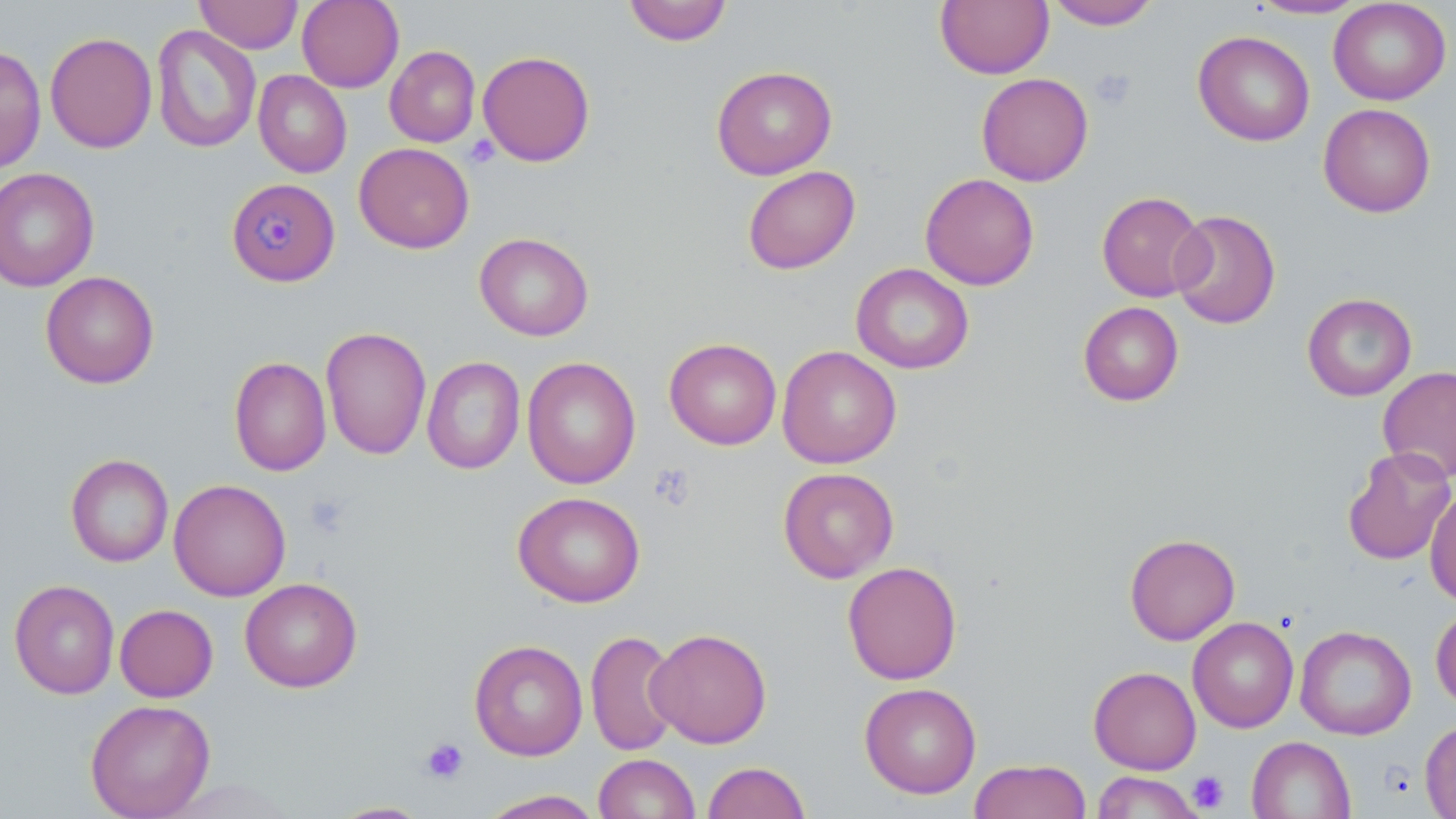

slide-level diagnosis = Plasmodium malariae
uninfected red blood cell locations = approximate bounding boxes as [x1, y1, x2, y2] in pixels: [194, 0, 303, 54], [296, 0, 404, 92], [1246, 0, 1370, 20], [1328, 0, 1451, 105], [622, 1, 733, 46], [935, 1, 1054, 79], [1045, 1, 1161, 30], [151, 24, 262, 154], [1193, 30, 1315, 146], [44, 31, 157, 154], [0, 45, 46, 174], [385, 45, 480, 147], [478, 50, 595, 166], [711, 65, 837, 180], [253, 70, 352, 178], [976, 72, 1093, 186], [1318, 103, 1436, 217], [353, 143, 474, 253], [742, 165, 860, 274], [0, 167, 99, 292], [920, 173, 1039, 290], [1097, 190, 1207, 302], [1169, 209, 1281, 329], [474, 232, 594, 341], [850, 263, 974, 374], [40, 271, 159, 388], [1302, 292, 1417, 401], [1078, 301, 1184, 406], [320, 326, 431, 460], [664, 337, 782, 450], [777, 345, 902, 469], [229, 356, 331, 477], [422, 356, 525, 474], [521, 357, 641, 489], [1378, 366, 1456, 483], [1342, 446, 1455, 565], [65, 453, 174, 567], [778, 466, 899, 583], [168, 479, 291, 601], [1425, 487, 1456, 607], [512, 491, 646, 607], [1124, 533, 1241, 645], [842, 560, 962, 685], [239, 577, 363, 693], [9, 579, 120, 699], [114, 604, 218, 702], [1430, 605, 1456, 710], [1188, 617, 1299, 733], [1294, 625, 1417, 740], [646, 627, 772, 748], [586, 629, 682, 757], [469, 640, 588, 761], [1089, 666, 1201, 774], [859, 682, 981, 799], [85, 699, 216, 819], [1419, 720, 1456, 818], [1246, 735, 1356, 819], [593, 753, 700, 818], [968, 759, 1091, 819], [703, 760, 810, 819], [1091, 771, 1204, 818], [477, 789, 605, 818], [326, 801, 434, 818]
preparation = thin blood smear
field of view = one of a larger specimen
Plasmodium malariae-infected red blood cell locations = approximate bounding boxes as [x1, y1, x2, y2] in pixels: [232, 183, 339, 285]
image size = 1456×819 pixels
magnification = 1000x
modality = optical microscopy
stain = May-Grünwald-Giemsa
platelet locations = approximate bounding boxes as [x1, y1, x2, y2] in pixels: [1089, 67, 1136, 111], [465, 134, 501, 168], [649, 463, 697, 511], [304, 494, 351, 539], [420, 737, 469, 784], [1188, 770, 1230, 813]